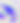

400x magnification. Toxoplasma gondii is shown. Micrograph.